Point out each Plasmodium parasite.
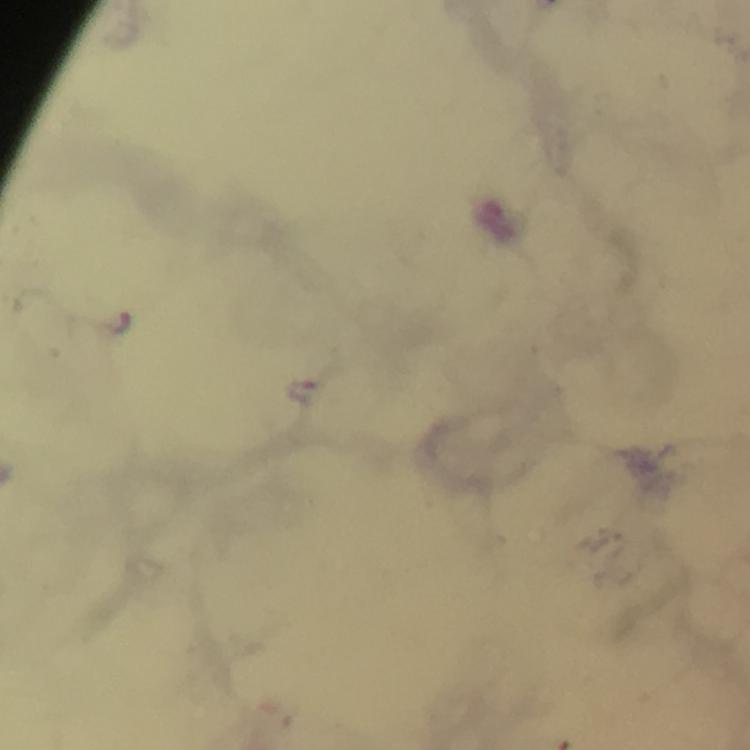

Approximate centers as [x, y] in pixels.
Plasmodium parasites: [116, 322], [302, 392].

Photographed through the microscope with a smartphone camera. At 100x magnification. Giemsa stain. Thick blood film. Cropped region of a single field of view. Immersion oil applied. Image is 750×750 pixels. From a diagnostic examination for malaria.